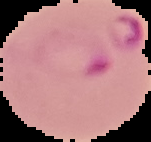

Malaria status: parasitized. From a thin blood smear. Segmented cell region on a black background. Image is 151×142 pixels.